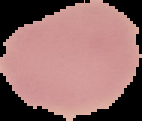
Summary:
  - Image size: 142×121 pixels
  - Preparation: thin blood film
  - Result: negative for malaria parasites
  - Image type: segmented cell region on a black background